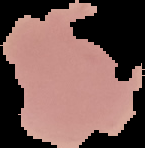 Segmented cell region on a black background. Result: no Plasmodium parasites detected. From a thin blood smear. Image is 145×148 pixels.